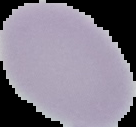 Result: no Plasmodium parasites detected. Image is 136×127 pixels. The area outside the segmented cell region is set to black. From a thin blood smear.